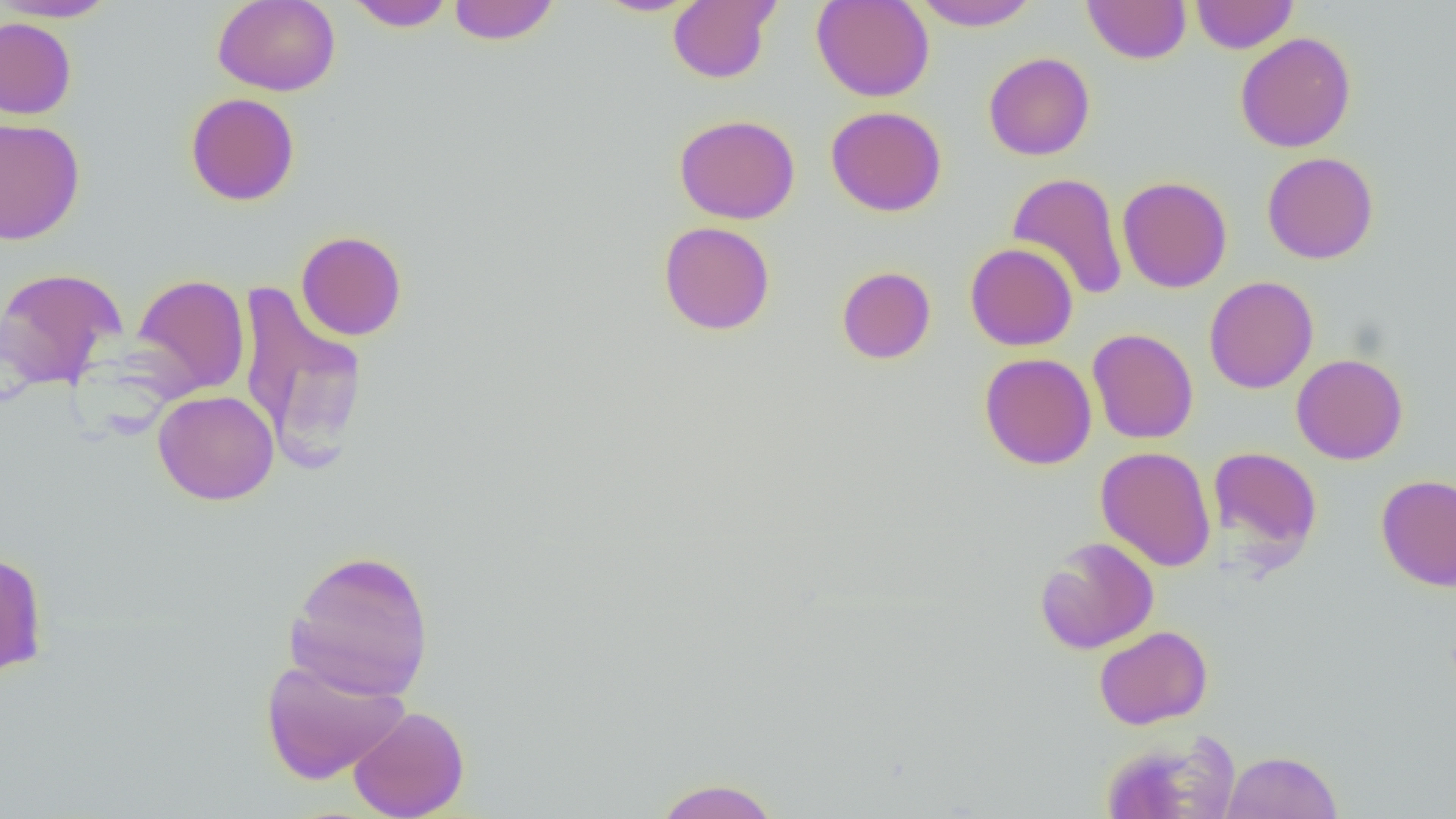

slide-level diagnosis = no evidence of blood parasites
uninfected red blood cell locations = approximate bounding boxes as (x1,y1)-(x2,y2) corner pairs in pixels: (0,0)-(120,22), (212,0)-(340,96), (447,0)-(561,45), (592,0)-(704,17), (668,0)-(780,84), (811,0)-(934,102), (1081,0)-(1191,64), (1190,0)-(1298,54), (346,1)-(455,31), (912,1)-(1039,30), (0,16)-(77,119), (1234,32)-(1357,153), (983,52)-(1095,161), (186,93)-(300,206), (825,105)-(947,216), (674,114)-(800,224), (0,117)-(85,246), (1262,152)-(1379,264), (1007,172)-(1128,300), (1117,176)-(1232,293), (659,221)-(775,335), (296,230)-(407,341), (965,242)-(1078,351), (836,266)-(936,364), (0,267)-(125,390), (129,273)-(250,398), (1204,276)-(1318,394), (236,282)-(368,464), (1088,328)-(1199,444), (979,352)-(1097,470), (1291,353)-(1408,464), (153,389)-(279,505), (1095,446)-(1217,572), (1208,446)-(1322,562), (1375,473)-(1456,592), (1034,537)-(1159,654), (286,549)-(435,700), (0,551)-(48,678), (1094,625)-(1212,730), (259,655)-(411,784), (348,706)-(470,819), (1099,730)-(1242,819), (1220,750)-(1343,819), (652,778)-(782,819)
magnification = 1000x
modality = light microscopy
field of view = one of a larger specimen
image size = 1456×819 pixels
preparation = thin blood film